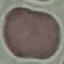
{
  "malaria_status": "uninfected",
  "image_type": "automatically extracted cell patch, resized to 64 × 64 pixels",
  "stain": "Giemsa",
  "capture": "smartphone through the microscope eyepiece",
  "preparation": "thin blood film"
}